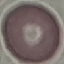
Summary:
  - Result: negative for malaria parasites
  - Capture: smartphone through the microscope eyepiece
  - Image type: automatically extracted cell patch, resized to 64 × 64 pixels
  - Preparation: thin blood smear
  - Stain: Giemsa